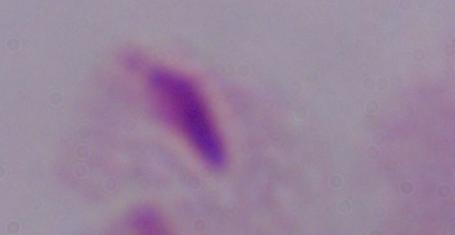

Summary:
  - Modality: micrograph
  - Magnification: 1000x
  - Identification: trichomonad